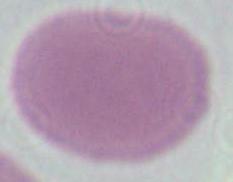

magnification = 1000x
modality = micrograph
identification = red blood cell